Comment on the morphology of the red blood cells.
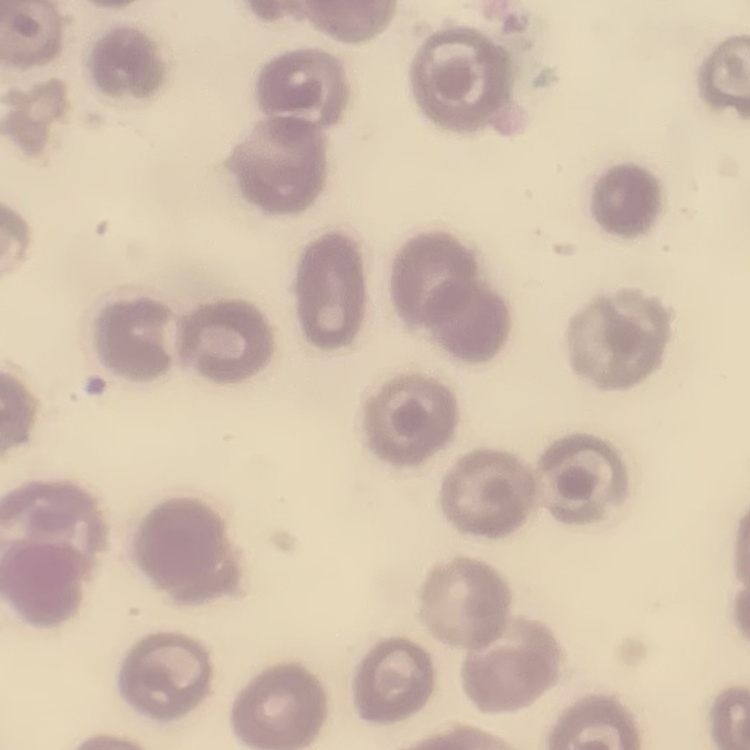

No rouleaux formation.

Summary:
  - Image type: square crop of a larger photomicrograph
  - Preparation: thin blood film
  - Stain: Field's or Giemsa